Assess this cell for malaria.
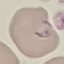
It is parasitized.

Summary:
  - Stain: Giemsa
  - Capture: smartphone through the microscope eyepiece
  - Preparation: thin smear
  - Image type: automatically extracted cell patch, resized to 64 × 64 pixels